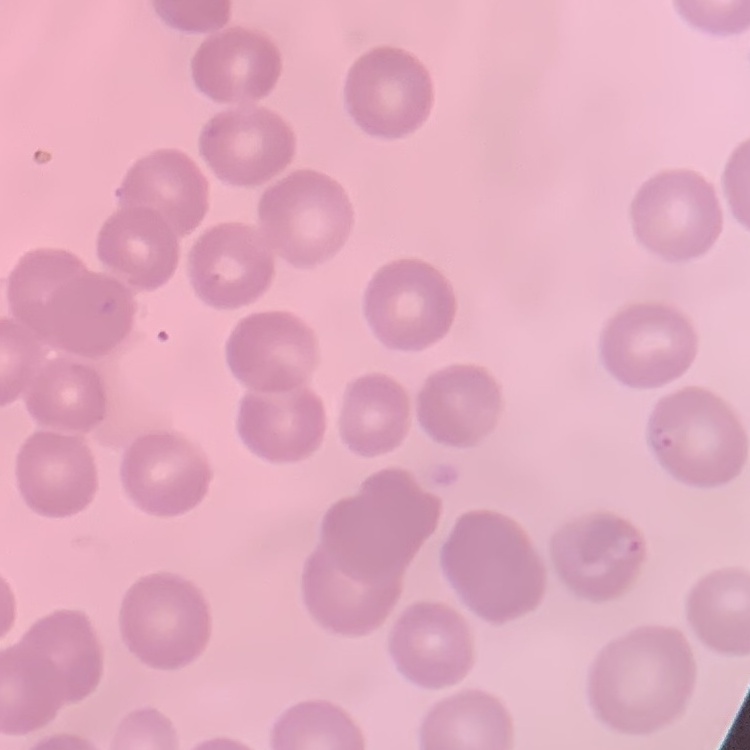
Summary:
  - Red blood cell morphology: no rouleaux formation
  - Stain: Field's or Giemsa
  - Image type: square crop of a larger photomicrograph
  - Preparation: thin blood smear